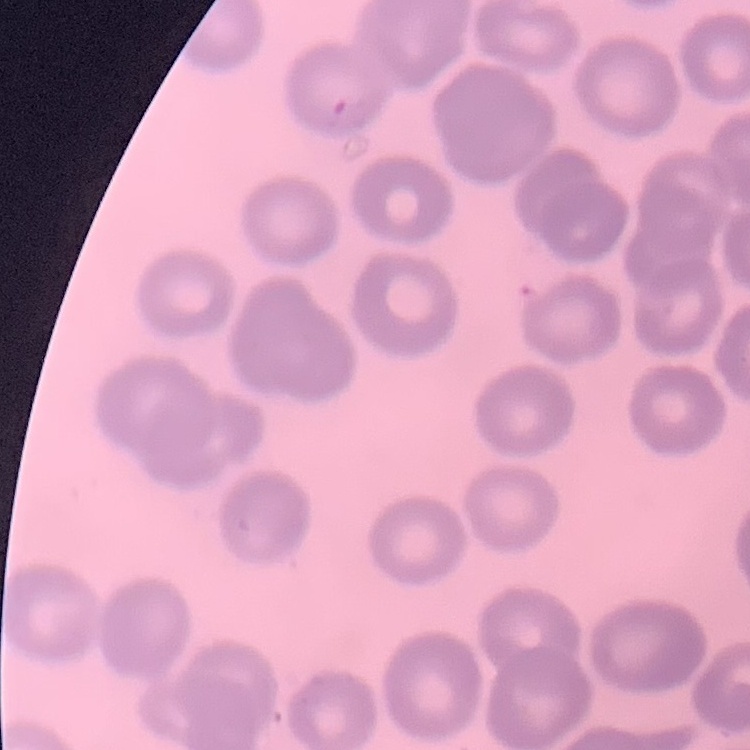
erythrocyte_morphology: no rouleaux formation
stain: Field's or Giemsa
preparation: thin peripheral smear
image_type: square crop of a larger photomicrograph